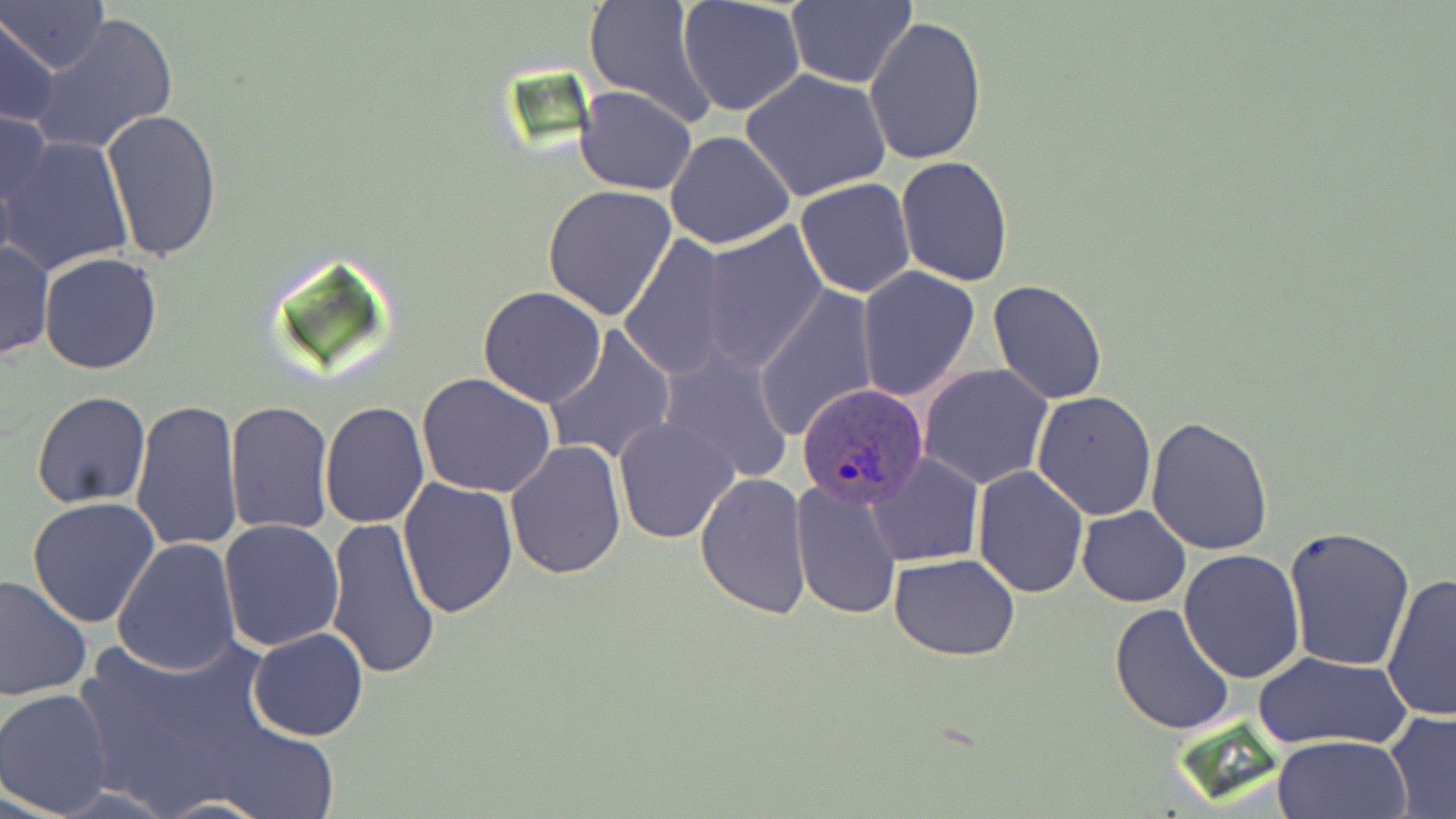 Approximate bounding boxes as (x1, y1, x2, y2) in pixels. Plasmodium ovale-infected red blood cell locations: (795, 382, 930, 509). Uninfected red blood cell locations: (0, 0, 108, 74), (678, 0, 807, 118), (784, 1, 918, 88), (582, 2, 719, 127), (0, 12, 61, 127), (29, 12, 179, 155), (865, 15, 988, 165), (741, 68, 892, 202), (575, 86, 697, 195), (0, 105, 54, 227), (102, 107, 222, 263), (664, 129, 795, 250), (2, 137, 134, 275), (896, 156, 1014, 285), (795, 178, 917, 297), (543, 184, 676, 321), (697, 220, 830, 372), (618, 236, 738, 380), (0, 238, 54, 364), (40, 252, 163, 374), (857, 266, 980, 401), (988, 280, 1108, 404), (756, 286, 878, 440), (477, 287, 607, 408), (442, 295, 593, 476), (546, 327, 675, 464), (659, 351, 795, 484), (918, 364, 1053, 489), (417, 374, 555, 499), (1031, 390, 1158, 521), (32, 391, 151, 508), (131, 397, 243, 554), (224, 401, 335, 536), (319, 401, 429, 529), (614, 417, 740, 544), (1146, 418, 1274, 556), (505, 439, 628, 579), (866, 453, 982, 566), (971, 467, 1088, 595), (694, 470, 812, 619), (398, 477, 521, 618), (790, 477, 903, 620), (28, 496, 161, 628), (1076, 506, 1191, 607), (323, 517, 441, 680), (219, 519, 346, 652), (1282, 525, 1418, 671), (112, 536, 242, 675), (1179, 549, 1306, 685), (889, 554, 1022, 659), (1381, 573, 1456, 721), (0, 574, 92, 702), (1111, 603, 1237, 736), (71, 623, 292, 815), (249, 627, 369, 742), (1252, 651, 1412, 750), (0, 688, 117, 815), (1383, 710, 1456, 818), (215, 721, 339, 818), (1270, 734, 1411, 819), (155, 798, 268, 818). Slide-level diagnosis: Plasmodium ovale. Optical microscopy. Captured at 1000x magnification. One field of a larger specimen. Thin blood film. May-Grünwald-Giemsa-stained preparation. Image is 1456×819 pixels.